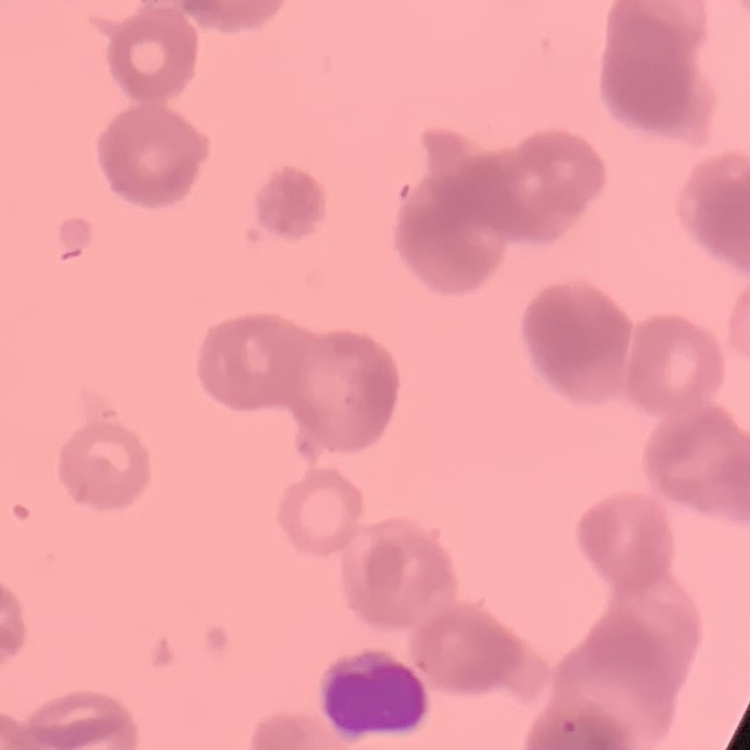

The red blood cells exhibit rouleaux formation. Thin peripheral smear. One tile cut from a larger photomicrograph. Field's or Giemsa stain.